Assess this cell for malaria.
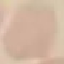
It is uninfected.

stain: Giemsa
image_type: cell patch, automatically extracted from a larger field of view and resized to 64 × 64 pixels
preparation: thin blood film
capture: smartphone through the microscope eyepiece